Assess this cell for malaria.
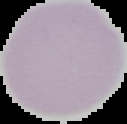
Uninfected.

Image is 127×124 pixels. From a thin blood smear. Segmented cell region on a black background.